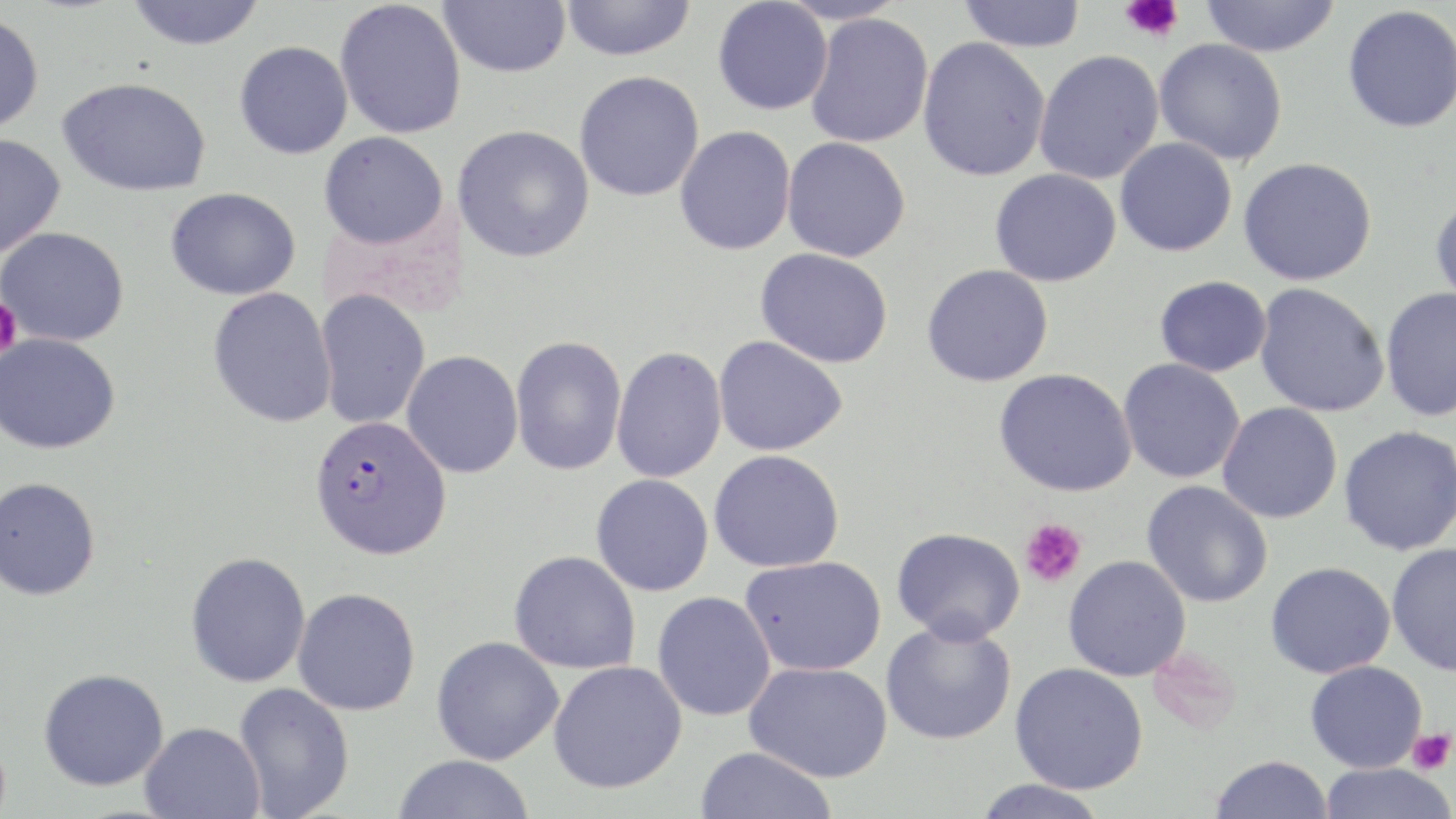
slide-level diagnosis = Plasmodium falciparum
magnification = 1000x
image size = 1456×819 pixels
preparation = thin blood film
stain = May-Grünwald-Giemsa
uninfected red blood cell locations = approximate bounding boxes as named x1/y1/x2/y2 corners in pixels: (x1=125, y1=0, x2=265, y2=50), (x1=560, y1=0, x2=696, y2=61), (x1=776, y1=0, x2=908, y2=25), (x1=958, y1=0, x2=1086, y2=52), (x1=1200, y1=0, x2=1340, y2=57), (x1=334, y1=1, x2=467, y2=139), (x1=439, y1=1, x2=571, y2=77), (x1=712, y1=1, x2=833, y2=116), (x1=1342, y1=4, x2=1456, y2=133), (x1=0, y1=12, x2=45, y2=134), (x1=805, y1=13, x2=934, y2=148), (x1=917, y1=36, x2=1051, y2=182), (x1=1154, y1=39, x2=1287, y2=165), (x1=234, y1=41, x2=353, y2=159), (x1=1034, y1=50, x2=1165, y2=185), (x1=574, y1=71, x2=705, y2=202), (x1=57, y1=77, x2=212, y2=197), (x1=453, y1=125, x2=595, y2=263), (x1=675, y1=126, x2=796, y2=256), (x1=319, y1=131, x2=448, y2=249), (x1=0, y1=133, x2=66, y2=258), (x1=782, y1=136, x2=911, y2=262), (x1=1115, y1=137, x2=1237, y2=256), (x1=1238, y1=157, x2=1377, y2=286), (x1=989, y1=168, x2=1122, y2=287), (x1=166, y1=187, x2=301, y2=300), (x1=1429, y1=192, x2=1456, y2=312), (x1=0, y1=226, x2=129, y2=346), (x1=755, y1=247, x2=894, y2=367), (x1=922, y1=264, x2=1054, y2=387), (x1=1154, y1=275, x2=1272, y2=377), (x1=1254, y1=283, x2=1390, y2=417), (x1=1379, y1=286, x2=1456, y2=423), (x1=207, y1=287, x2=337, y2=428), (x1=314, y1=288, x2=431, y2=430), (x1=0, y1=333, x2=121, y2=454), (x1=510, y1=335, x2=627, y2=476), (x1=713, y1=336, x2=848, y2=456), (x1=612, y1=347, x2=727, y2=484), (x1=401, y1=351, x2=523, y2=479), (x1=1118, y1=358, x2=1245, y2=484), (x1=994, y1=368, x2=1137, y2=496), (x1=1217, y1=402, x2=1342, y2=523), (x1=1338, y1=425, x2=1456, y2=556), (x1=708, y1=450, x2=845, y2=573), (x1=590, y1=474, x2=714, y2=596), (x1=0, y1=476, x2=101, y2=600), (x1=1142, y1=480, x2=1273, y2=607), (x1=892, y1=526, x2=1025, y2=644), (x1=1386, y1=542, x2=1456, y2=676), (x1=509, y1=550, x2=641, y2=674), (x1=185, y1=551, x2=311, y2=688), (x1=740, y1=555, x2=887, y2=676), (x1=1063, y1=555, x2=1191, y2=681), (x1=1266, y1=561, x2=1395, y2=678), (x1=292, y1=587, x2=421, y2=716), (x1=652, y1=591, x2=776, y2=721), (x1=881, y1=618, x2=1016, y2=745), (x1=431, y1=636, x2=563, y2=765), (x1=548, y1=660, x2=687, y2=794), (x1=1305, y1=660, x2=1427, y2=773), (x1=1010, y1=661, x2=1149, y2=795), (x1=744, y1=662, x2=892, y2=782), (x1=37, y1=668, x2=169, y2=792), (x1=233, y1=682, x2=354, y2=818), (x1=139, y1=721, x2=265, y2=819), (x1=694, y1=746, x2=838, y2=819), (x1=391, y1=755, x2=537, y2=818), (x1=1209, y1=755, x2=1334, y2=819), (x1=1318, y1=762, x2=1455, y2=819), (x1=972, y1=779, x2=1110, y2=819)
platelet locations = approximate bounding boxes as named x1/y1/x2/y2 corners in pixels: (x1=1120, y1=0, x2=1184, y2=42), (x1=0, y1=297, x2=21, y2=358), (x1=1020, y1=518, x2=1087, y2=587), (x1=1407, y1=729, x2=1454, y2=774)
field of view = single
Plasmodium falciparum-infected red blood cell locations = approximate bounding boxes as named x1/y1/x2/y2 corners in pixels: (x1=309, y1=416, x2=452, y2=560)
modality = optical microscopy